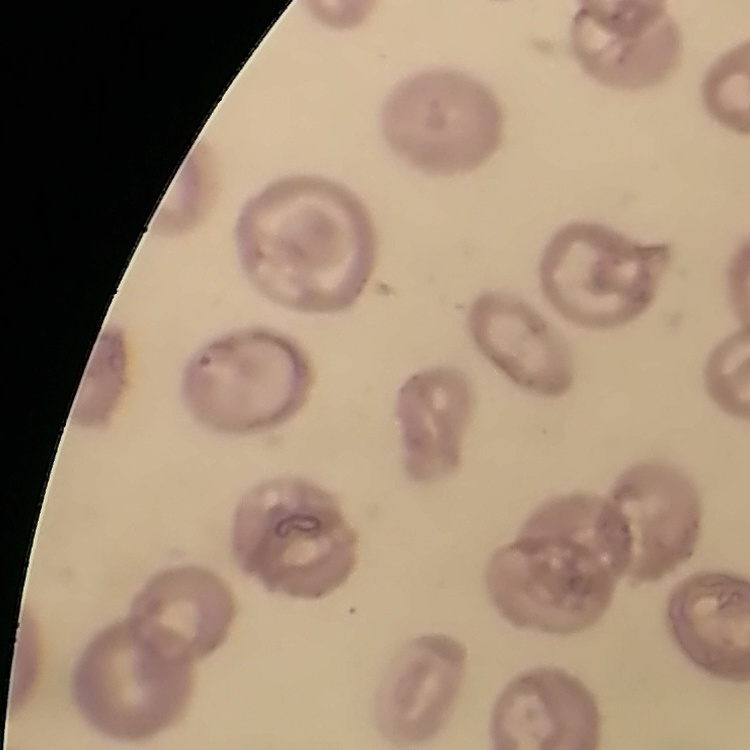
The erythrocytes exhibit no rouleaux formation. One tile cut from a larger photomicrograph. Thin blood film. Stained with either Field's or Giemsa.